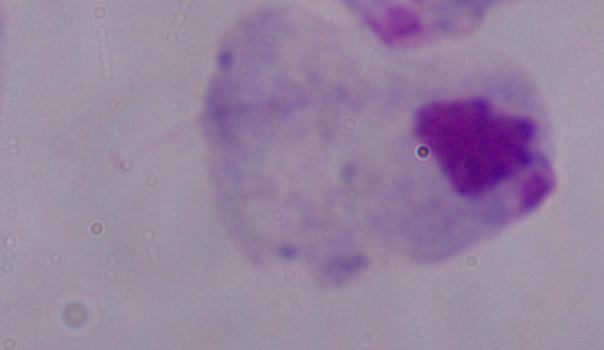

Summary:
  - Magnification: 1000x
  - Modality: photomicrograph
  - Identification: trichomonad